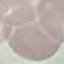

Summary:
  - Result: no malaria parasites detected
  - Preparation: thin blood film
  - Capture: smartphone camera at the microscope eyepiece
  - Stain: Giemsa
  - Image type: automatically extracted cell patch, resized to 64 × 64 pixels